Assess the morphology of the erythrocytes.
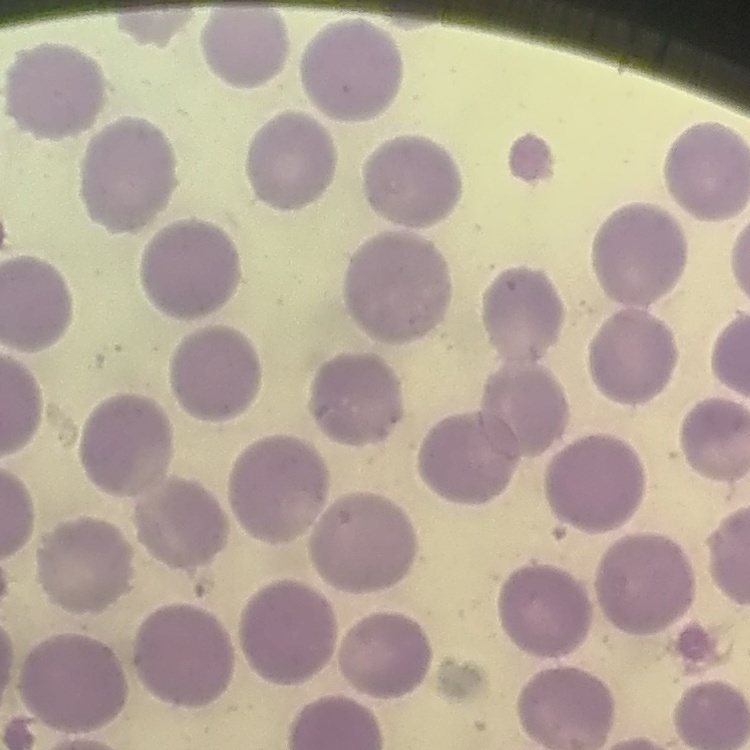

They show no rouleaux formation.

image type = square crop of a larger photomicrograph
stain = Field's or Giemsa
preparation = thin blood smear